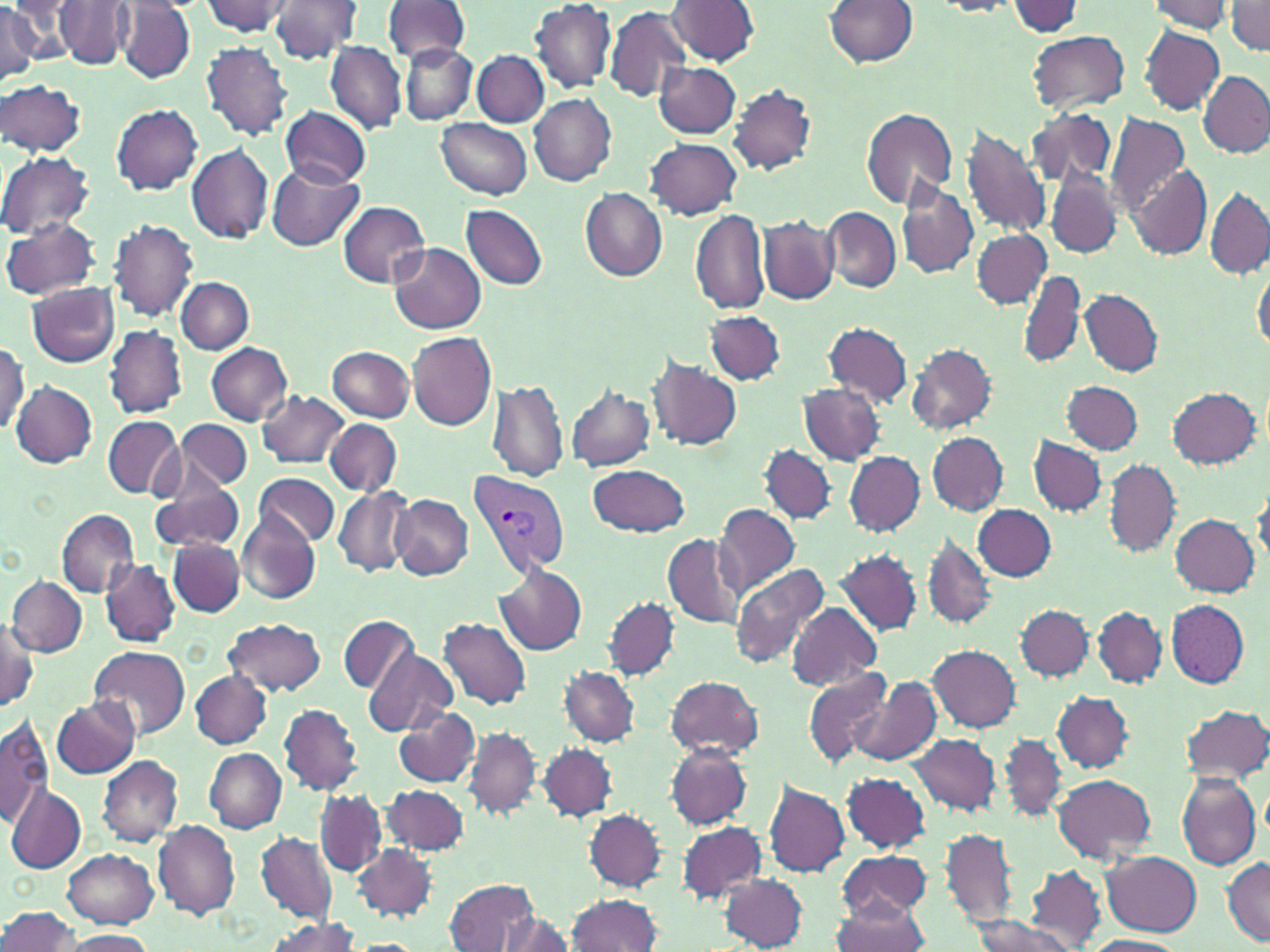

Summary:
  - Coordinate format: approximate bounding boxes as [x1, y1, x2, y2] in pixels
  - Plasmodium vivax-infected red blood cell locations: [467, 467, 571, 578]
  - Uninfected red blood cell locations: [7, 0, 79, 60], [202, 0, 293, 36], [268, 0, 362, 62], [383, 0, 470, 64], [531, 0, 616, 93], [667, 0, 758, 65], [824, 0, 917, 67], [1227, 0, 1270, 52], [932, 1, 1019, 16], [1147, 1, 1234, 34], [53, 2, 136, 70], [114, 2, 196, 84], [1008, 2, 1086, 38], [0, 3, 42, 81], [606, 7, 692, 103], [1139, 25, 1225, 113], [1026, 30, 1129, 113], [202, 41, 292, 140], [327, 41, 405, 132], [399, 42, 476, 124], [473, 50, 549, 127], [655, 62, 740, 138], [1199, 70, 1270, 158], [0, 80, 87, 157], [730, 83, 817, 175], [528, 93, 617, 185], [111, 103, 202, 195], [280, 106, 372, 189], [862, 107, 959, 209], [1025, 108, 1118, 188], [1105, 113, 1188, 219], [436, 117, 532, 198], [961, 123, 1051, 239], [646, 139, 741, 220], [186, 144, 274, 245], [0, 151, 93, 238], [268, 163, 364, 251], [1129, 165, 1210, 258], [1047, 167, 1123, 260], [896, 178, 980, 280], [580, 187, 667, 281], [1206, 187, 1270, 278], [338, 202, 430, 288], [462, 204, 547, 289], [822, 206, 901, 292], [689, 210, 771, 314], [758, 215, 839, 305], [3, 217, 102, 301], [109, 219, 198, 321], [973, 229, 1051, 308], [390, 242, 486, 334], [1253, 262, 1270, 355], [1019, 270, 1087, 370], [177, 276, 254, 354], [28, 283, 120, 367], [1079, 290, 1163, 377], [705, 311, 785, 386], [824, 322, 914, 406], [105, 326, 188, 418], [408, 331, 496, 432], [0, 340, 28, 438], [907, 342, 999, 435], [207, 343, 293, 425], [328, 346, 414, 421], [647, 357, 742, 451], [488, 379, 568, 482], [11, 380, 97, 468], [1062, 380, 1143, 454], [798, 382, 884, 465], [566, 383, 656, 472], [1167, 385, 1262, 468], [258, 391, 349, 468], [103, 416, 183, 498], [325, 418, 401, 496], [177, 420, 253, 491], [928, 432, 1008, 515], [1029, 436, 1106, 516], [758, 443, 838, 525], [846, 452, 924, 537], [1103, 460, 1182, 557], [587, 463, 691, 538], [253, 471, 339, 548], [148, 479, 247, 554], [334, 487, 413, 577], [392, 495, 474, 579], [714, 504, 800, 597], [975, 505, 1057, 581], [57, 509, 139, 596], [1169, 513, 1259, 596], [237, 515, 320, 604], [921, 533, 997, 630], [661, 534, 745, 628], [168, 538, 245, 616], [833, 549, 923, 637], [100, 557, 180, 648], [730, 563, 831, 669], [494, 564, 589, 656], [7, 575, 86, 656], [603, 596, 678, 680], [1167, 601, 1250, 687], [787, 603, 881, 691], [1015, 603, 1095, 682], [1093, 605, 1166, 688], [341, 615, 418, 693], [438, 616, 531, 709], [1, 618, 39, 713], [224, 618, 326, 696], [88, 645, 189, 740], [929, 645, 1020, 732], [363, 648, 457, 735], [561, 666, 640, 746], [803, 666, 895, 767], [190, 669, 272, 748], [665, 674, 763, 760], [847, 677, 941, 768], [1052, 691, 1133, 772], [51, 697, 140, 777], [1180, 703, 1270, 784], [279, 704, 362, 795], [393, 707, 481, 787], [0, 717, 53, 827], [464, 724, 541, 820], [907, 732, 1002, 816], [998, 733, 1067, 822], [538, 741, 618, 822], [665, 744, 755, 830], [205, 749, 286, 832], [97, 756, 184, 846], [843, 772, 930, 853], [1175, 772, 1261, 870], [1052, 773, 1155, 862], [764, 780, 850, 877], [5, 783, 85, 874], [383, 785, 469, 854], [314, 789, 388, 877], [584, 809, 665, 891], [152, 819, 240, 919], [674, 821, 768, 903], [941, 827, 1019, 927], [252, 830, 339, 925], [351, 843, 437, 919], [63, 849, 159, 929], [838, 849, 931, 923], [1101, 852, 1202, 936], [1221, 854, 1270, 945], [1025, 865, 1106, 949], [719, 874, 809, 950], [446, 878, 540, 952], [565, 894, 663, 951], [833, 899, 929, 952], [0, 906, 79, 952], [500, 912, 574, 951], [969, 915, 1079, 952], [263, 919, 360, 951], [58, 929, 155, 951], [1082, 935, 1184, 952], [354, 938, 421, 951]
  - Slide-level diagnosis: Plasmodium vivax
  - Modality: optical microscopy
  - Stain: May-Grünwald-Giemsa
  - Image size: 1270×952 pixels
  - Magnification: 1000x
  - Preparation: thin blood smear
  - Field of view: single